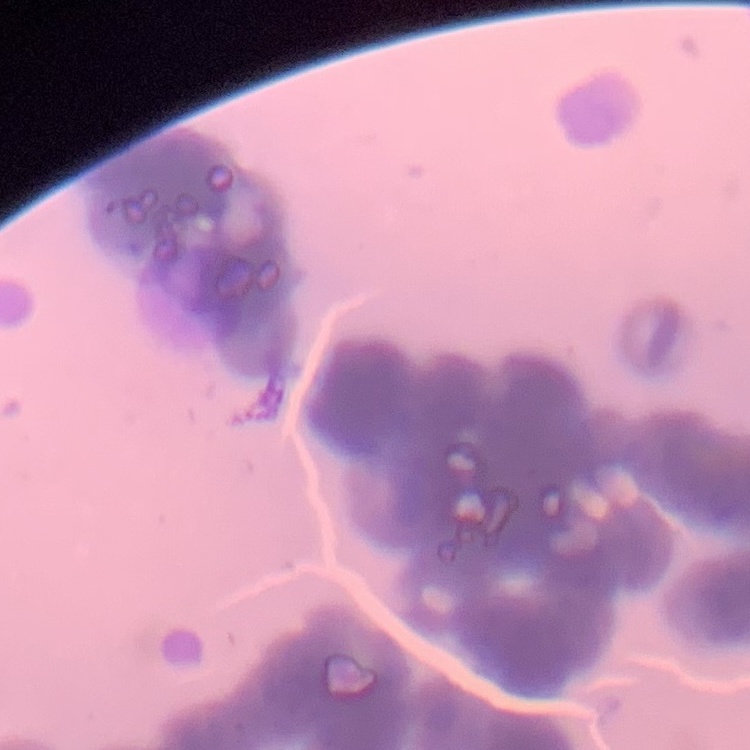
{
  "red_blood_cell_morphology": "rouleaux formation",
  "stain": "Field's or Giemsa",
  "preparation": "thin peripheral smear",
  "image_type": "one tile cut from a larger photomicrograph"
}